Classify this cell by malaria status.
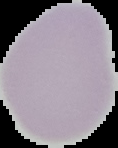
It is uninfected.

Summary:
  - Image type: cell region segmented out of the field of view; surrounding area masked to black
  - Preparation: thin blood smear
  - Image size: 118×148 pixels